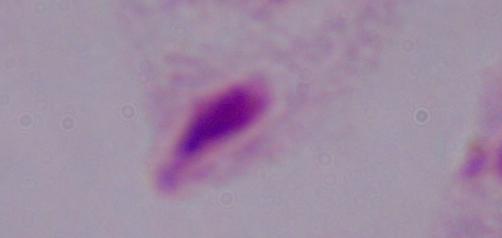
Photomicrograph. Captured at 1000x magnification. A trichomonad is shown.